Assess this cell for malaria.
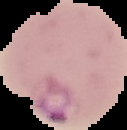
It is parasitized.

image type = segmented cell region on a black background
preparation = thin blood smear
image size = 127×130 pixels